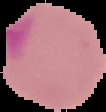
Summary:
  - Image size: 106×112 pixels
  - Preparation: thin blood film
  - Malaria status: parasitized
  - Image type: segmented cell region on a black background